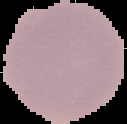

Summary:
  - Malaria status: uninfected
  - Preparation: thin blood film
  - Image type: segmented cell region with the area outside set to black
  - Image size: 127×124 pixels